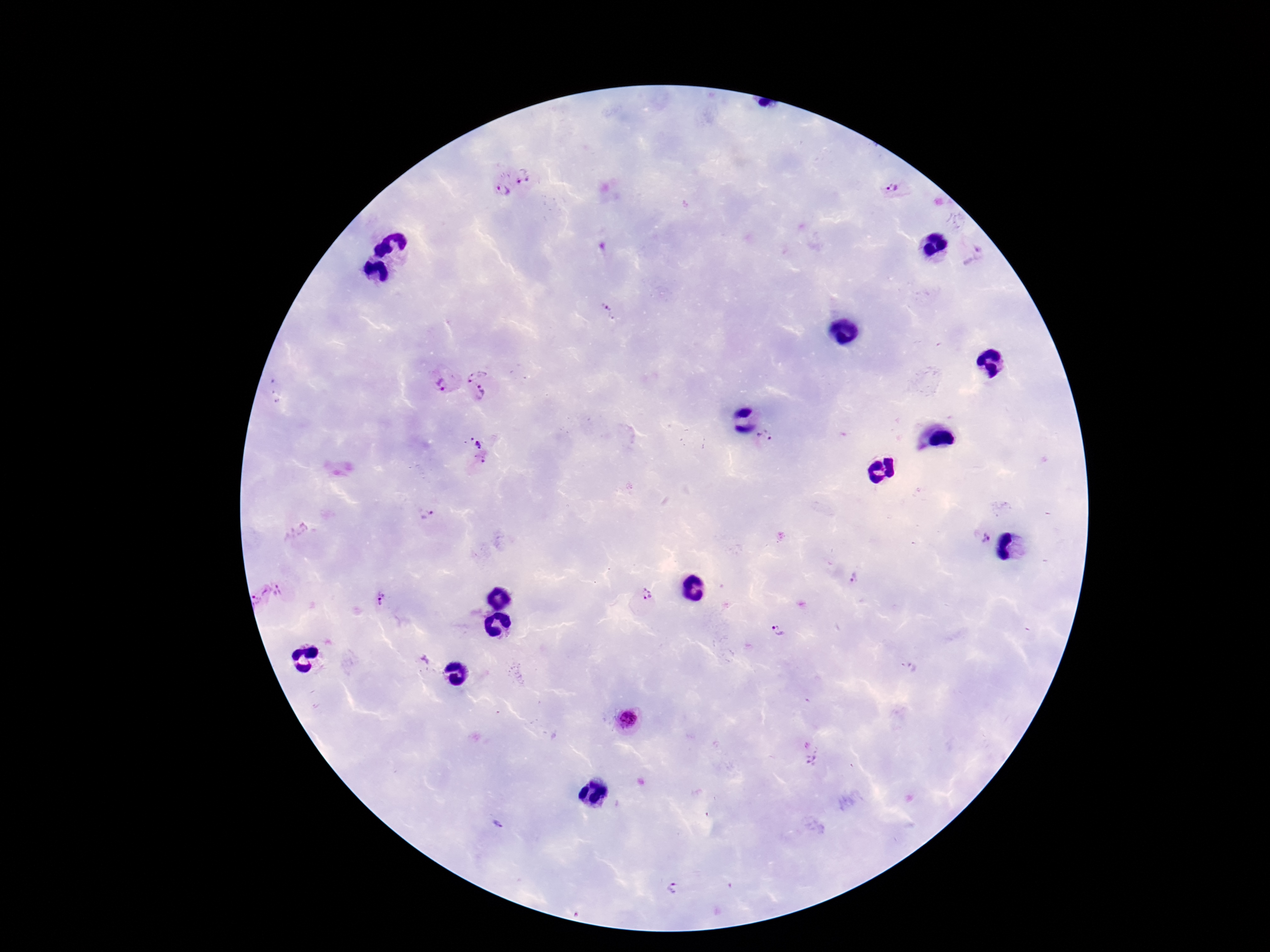
Approximate centers as (x, y) in pixels. Plasmodium parasite locations: (524, 176), (893, 190), (502, 191), (975, 255), (607, 311), (473, 370), (443, 382), (480, 393), (767, 438), (477, 450), (425, 514), (982, 537), (854, 579), (281, 592), (645, 595), (258, 598), (383, 598), (778, 630), (628, 719), (809, 752), (501, 824), (674, 889). 100x magnification. Giemsa stain. Thick blood film. Photographed through the microscope eyepiece with a smartphone camera. Patient malaria status: positive. Image is 1270×952 pixels. Single field of view.